Classify this cell by malaria status.
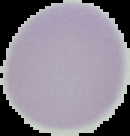
Uninfected.

preparation = thin blood film
image size = 130×136 pixels
image type = cell region segmented out of the field of view; surrounding area masked to black